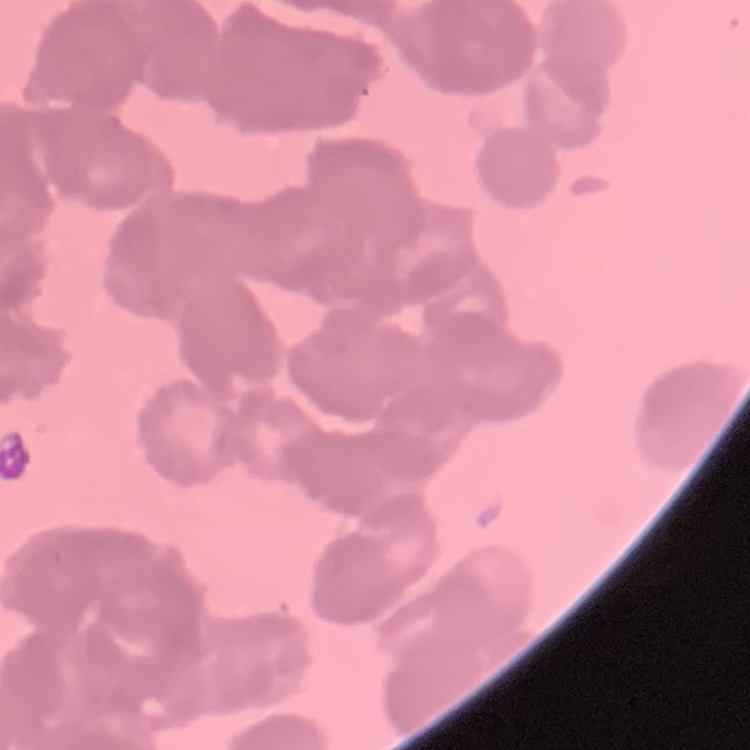
Summary:
  - Erythrocyte morphology: rouleaux formation
  - Image type: square crop of a larger photomicrograph
  - Stain: Field's or Giemsa
  - Preparation: thin blood smear